Give the position of every leukocyte visible.
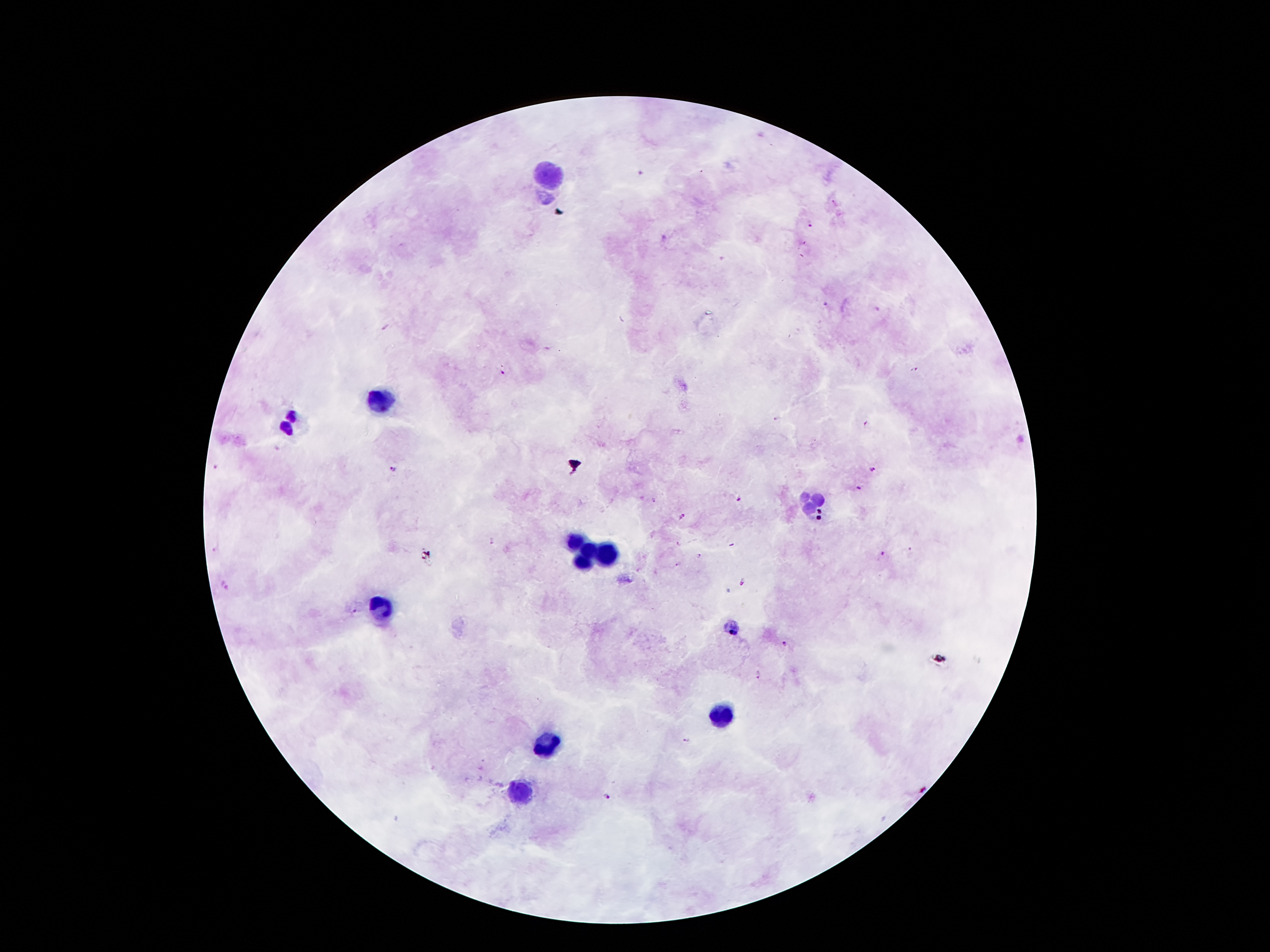
Approximate object centers, in pixels from the top-left corner.
Leukocytes: (x=546, y=173), (x=384, y=397), (x=290, y=422), (x=813, y=504), (x=577, y=541), (x=589, y=549), (x=608, y=555), (x=579, y=560), (x=381, y=608), (x=724, y=715), (x=546, y=746), (x=521, y=794).

Malaria parasite locations: (x=835, y=203), (x=809, y=222), (x=825, y=304), (x=914, y=369), (x=502, y=372), (x=777, y=418), (x=866, y=425), (x=217, y=467), (x=393, y=469), (x=871, y=470), (x=856, y=488), (x=739, y=498), (x=653, y=501), (x=680, y=517), (x=492, y=540), (x=679, y=545), (x=214, y=550), (x=881, y=554), (x=698, y=555), (x=678, y=563), (x=742, y=582), (x=224, y=583), (x=354, y=614), (x=734, y=628), (x=785, y=643), (x=758, y=674), (x=687, y=742), (x=605, y=797). Patient malaria status: positive for Plasmodium falciparum. Single field of view. Smartphone photograph taken through the microscope eyepiece. Thick peripheral-blood smear. 100x magnification. Giemsa stain. Image is 1270×952 pixels.